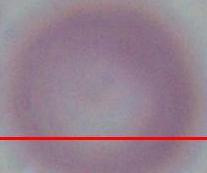

identification = erythrocyte
modality = micrograph
magnification = 1000x